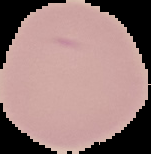

From a thin blood smear. Image is 151×154 pixels. Result: no Plasmodium parasites detected. The area outside the segmented cell region is set to black.